Report the malaria status of this cell.
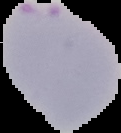
Parasitized.

{
  "image_type": "segmented cell region on a black background",
  "preparation": "thin blood film",
  "image_size": "121×133 pixels"
}